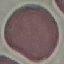
Result: no malaria parasites seen. Photographed with a smartphone camera at the microscope eyepiece. Automatically extracted cell patch, resized to 64 × 64 pixels. Giemsa-stained preparation. Thin blood smear.